Report the malaria status.
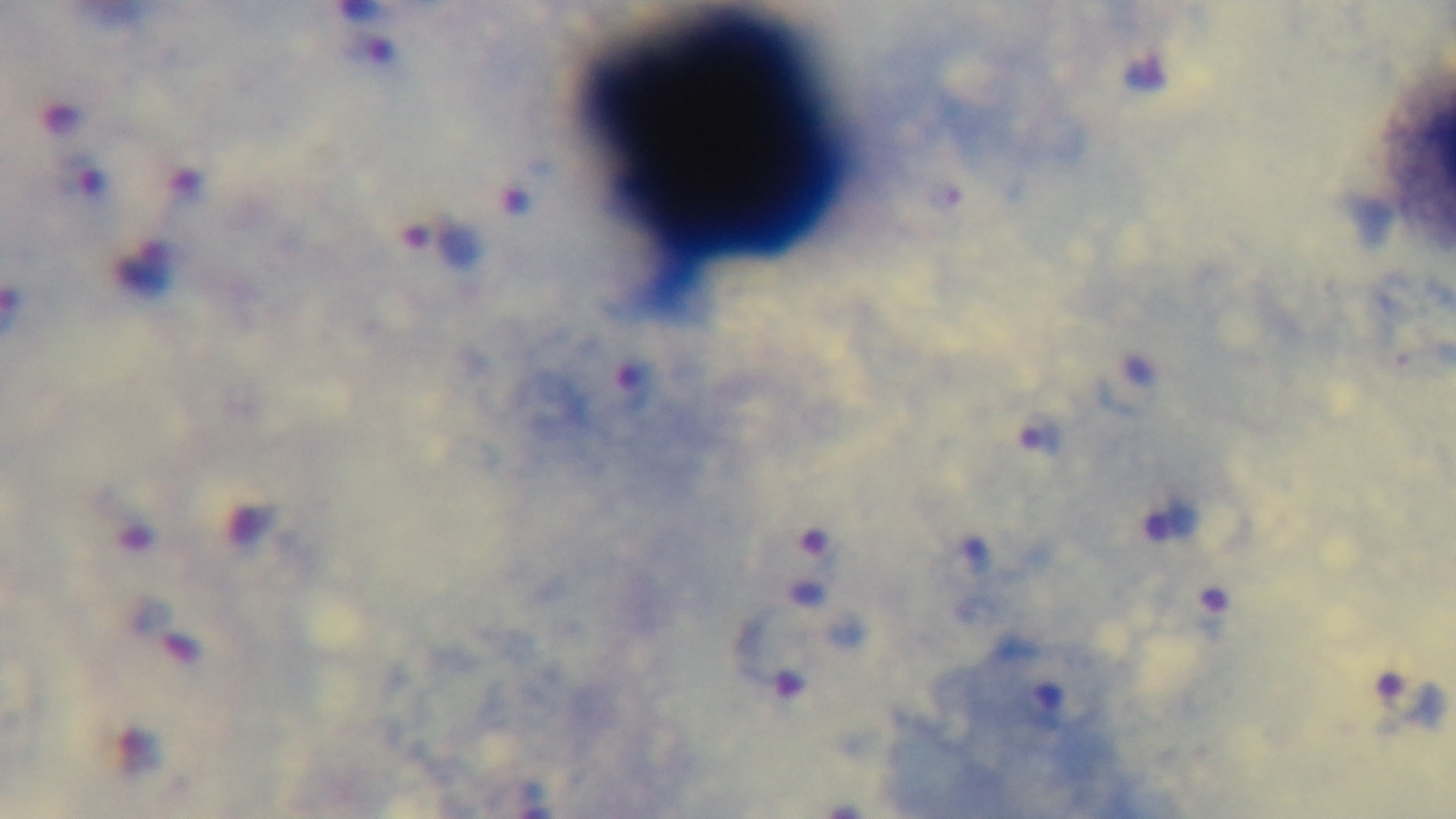
It is infected.

stain: Giemsa
capture: mounted 4K digital camera
preparation: thick blood film
modality: light microscopy
objective: 100x oil immersion
field_of_view: single